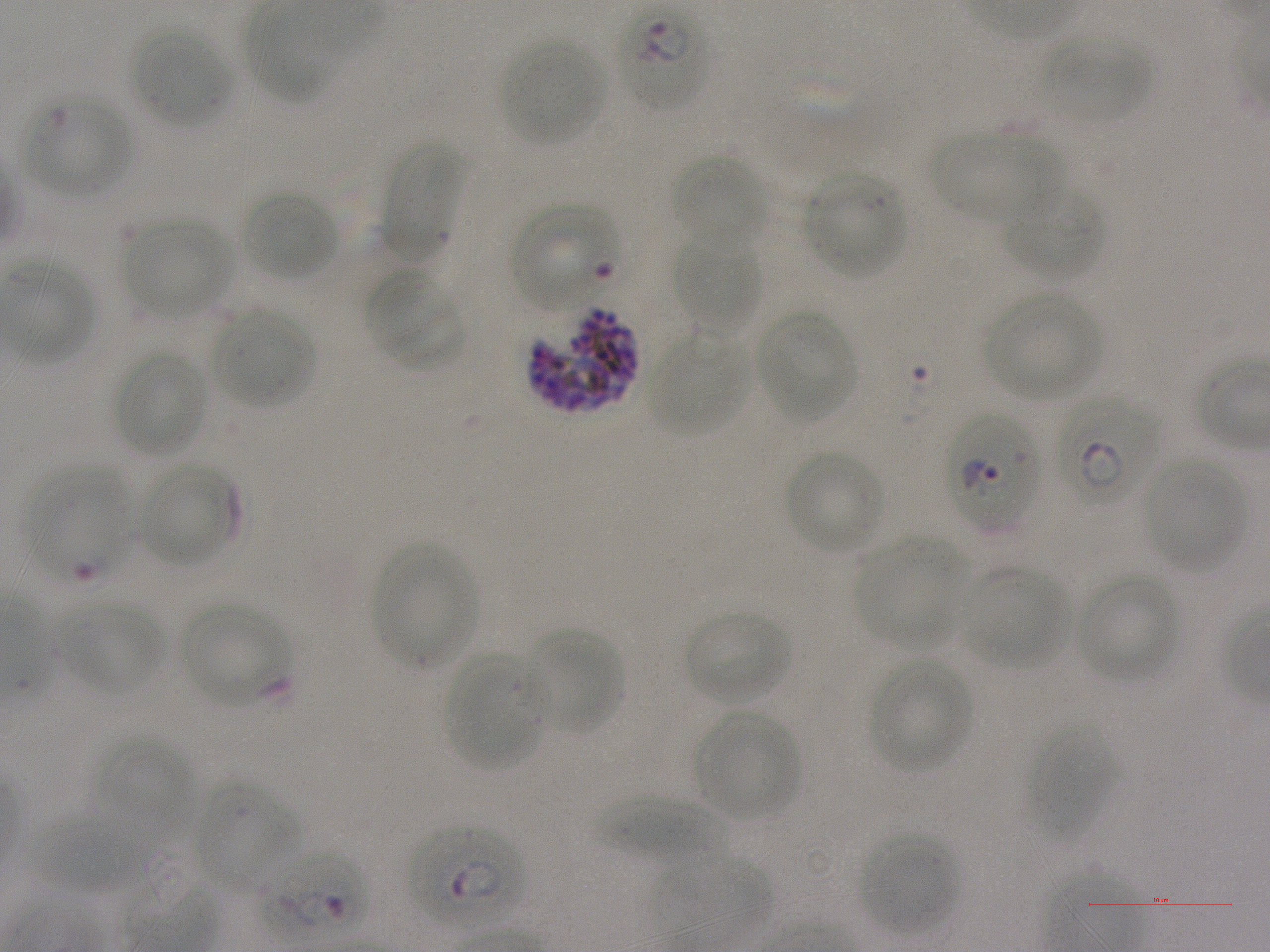
Not every red blood cell is marked. A life-cycle stage — or a range of stages, where the recorded stages span more than one — follows each staged infected red blood cell.
culture = in-vitro Plasmodium falciparum strain NF54, static
objective = 100x, oil immersion, numerical aperture 1.25
preparation = thin blood smear
donor blood group = A+
locations of red blood cells of indeterminate infection status = approximate bounding boxes as (x1, y1, x2, y2) in pixels: (25, 97, 133, 196), (512, 203, 616, 311), (530, 309, 638, 413), (947, 410, 1042, 532), (22, 464, 134, 583)
locations of infected red blood cells = approximate bounding boxes as (x1, y1, x2, y2) in pixels: (616, 4, 710, 111) early ring to early trophozoite; (1056, 396, 1160, 501) early ring to early trophozoite; (406, 823, 524, 928) ring; (255, 849, 369, 941) ring
stain = Giemsa
locations of uninfected red blood cells = approximate bounding boxes as (x1, y1, x2, y2) in pixels: (249, 12, 338, 105), (133, 29, 229, 126), (1038, 31, 1152, 120), (499, 38, 607, 145), (933, 128, 1057, 224), (381, 140, 463, 259), (672, 154, 768, 249), (805, 173, 905, 279), (1002, 187, 1106, 282), (241, 189, 339, 281), (124, 215, 233, 317), (673, 233, 762, 333), (366, 273, 464, 368), (986, 290, 1104, 401), (214, 308, 315, 408), (754, 309, 858, 424), (649, 334, 745, 437), (114, 351, 208, 457), (784, 450, 884, 554), (1143, 458, 1246, 571), (138, 463, 237, 567), (853, 539, 966, 649), (372, 542, 476, 666), (962, 568, 1069, 670), (1077, 575, 1180, 680), (61, 601, 165, 696), (179, 602, 292, 706), (683, 608, 790, 705), (523, 627, 624, 731), (443, 654, 547, 771), (869, 658, 972, 773), (693, 709, 801, 821), (1026, 720, 1117, 842), (94, 737, 193, 826), (193, 782, 299, 892), (598, 795, 727, 864), (27, 812, 164, 905), (860, 833, 961, 934), (651, 851, 772, 939)
image size = 1270×952 pixels
field of view = single